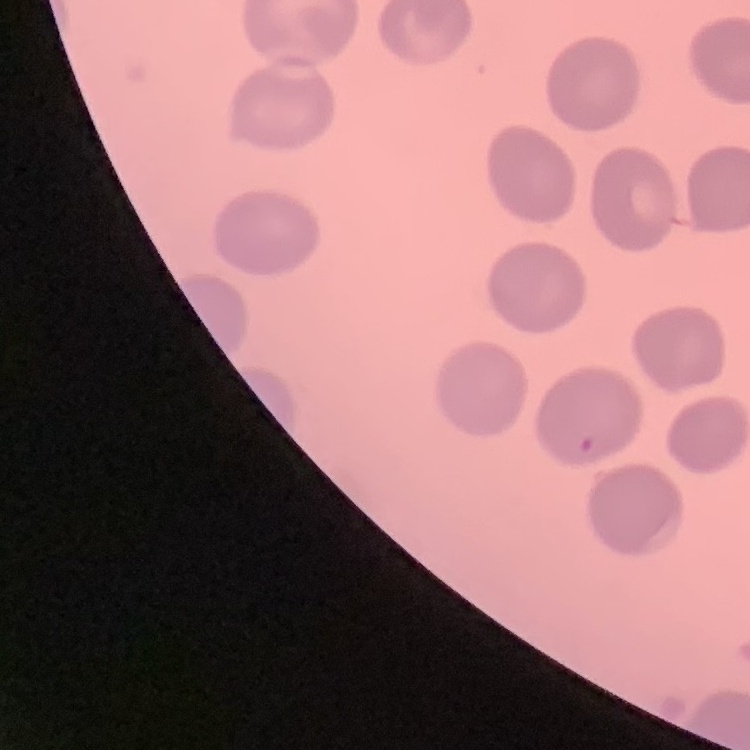
The erythrocytes show no rouleaux formation. One tile cut from a larger photomicrograph. Field's or Giemsa stain. Thin blood smear.